Point out each malaria parasite.
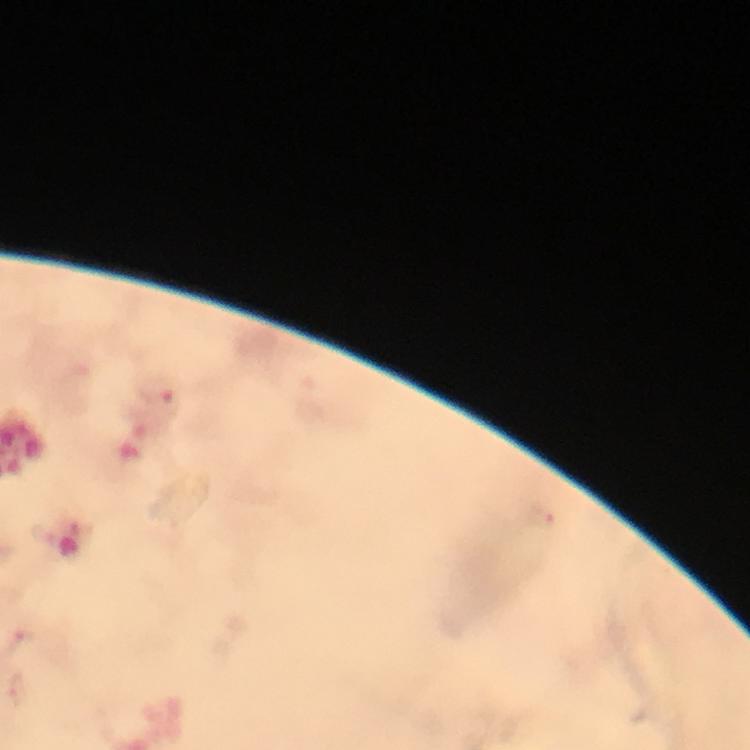

Approximate centers as [x, y] in pixels.
Malaria parasites: [158, 389], [21, 640], [15, 690].

Photographed through the microscope with a smartphone camera. At 100x magnification. Immersion oil applied. Giemsa stain. From a malaria diagnostic workup. A crop from one field of view. Thick smear. Image is 750×750 pixels.